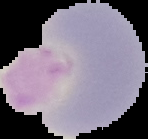
Image is 148×139 pixels. The area outside the segmented cell region is set to black. Malaria status: uninfected. From a thin blood smear.